State the blood parasite species.
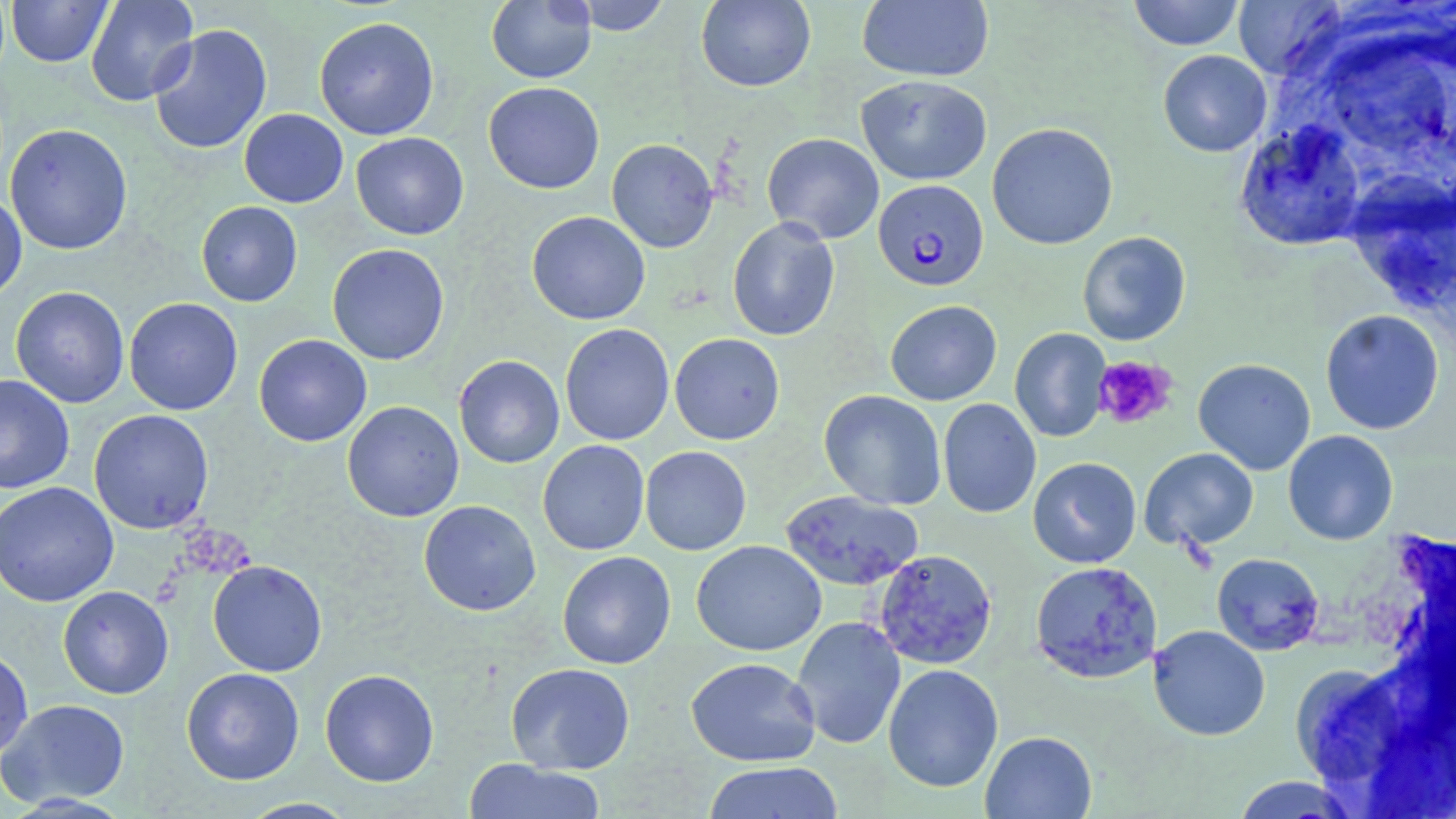

Plasmodium falciparum.

Summary:
  - Coordinate format: approximate bounding boxes as (x1, y1, x2, y2) in pixels
  - Uninfected red blood cell locations: (85, 0, 199, 106), (486, 0, 597, 84), (569, 0, 672, 35), (857, 0, 994, 83), (1127, 0, 1246, 50), (6, 1, 114, 67), (696, 1, 815, 92), (1233, 1, 1346, 79), (314, 16, 439, 140), (148, 24, 273, 155), (1157, 49, 1272, 157), (856, 74, 993, 185), (483, 82, 605, 194), (239, 109, 348, 208), (987, 122, 1118, 250), (1235, 122, 1367, 251), (5, 123, 132, 255), (351, 132, 469, 240), (762, 133, 884, 244), (606, 138, 718, 253), (0, 192, 27, 304), (196, 201, 303, 307), (526, 211, 651, 325), (727, 217, 840, 341), (1077, 231, 1191, 346), (327, 243, 450, 365), (10, 286, 130, 408), (124, 297, 243, 415), (885, 300, 1002, 405), (1319, 309, 1445, 435), (560, 323, 675, 445), (1009, 328, 1111, 443), (669, 333, 785, 445), (253, 334, 372, 446), (453, 355, 565, 468), (1193, 358, 1316, 475), (0, 374, 75, 494), (819, 390, 946, 510), (938, 398, 1041, 518), (341, 401, 465, 522), (89, 409, 214, 534), (1283, 430, 1398, 545), (538, 440, 650, 555), (640, 445, 752, 555), (1139, 447, 1259, 551), (1028, 457, 1142, 569), (0, 481, 119, 607), (780, 490, 924, 591), (418, 500, 541, 616), (691, 540, 827, 656), (874, 549, 997, 669), (557, 551, 676, 669), (1211, 552, 1324, 655), (208, 560, 327, 676), (1030, 561, 1163, 684), (58, 585, 173, 699), (790, 616, 906, 750), (1148, 625, 1270, 740), (0, 647, 34, 762), (685, 657, 821, 766), (505, 662, 636, 774), (882, 663, 1003, 793), (181, 667, 305, 785), (320, 668, 439, 787), (1, 698, 130, 808), (980, 730, 1097, 818), (462, 758, 608, 818), (701, 761, 845, 818), (1229, 775, 1362, 817), (238, 797, 359, 818)
  - Platelet locations: (1094, 355, 1178, 429)
  - Plasmodium falciparum-infected red blood cell locations: (873, 179, 989, 291)
  - Modality: optical microscopy
  - Magnification: 1000x
  - Preparation: thin blood smear
  - Image size: 1456×819 pixels
  - Stain: May-Grünwald-Giemsa
  - Field of view: single